Classify this cell by malaria status.
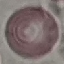
Uninfected.

{
  "stain": "Giemsa",
  "capture": "smartphone camera at the microscope eyepiece",
  "preparation": "thin blood smear",
  "image_type": "automatically extracted cell patch, resized to 64 × 64 pixels"
}